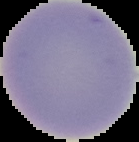
Summary:
  - Preparation: thin blood film
  - Malaria status: uninfected
  - Image type: cell region segmented out of the field of view; surrounding area masked to black
  - Image size: 139×142 pixels